Outline each Plasmodium falciparum-infected red blood cell.
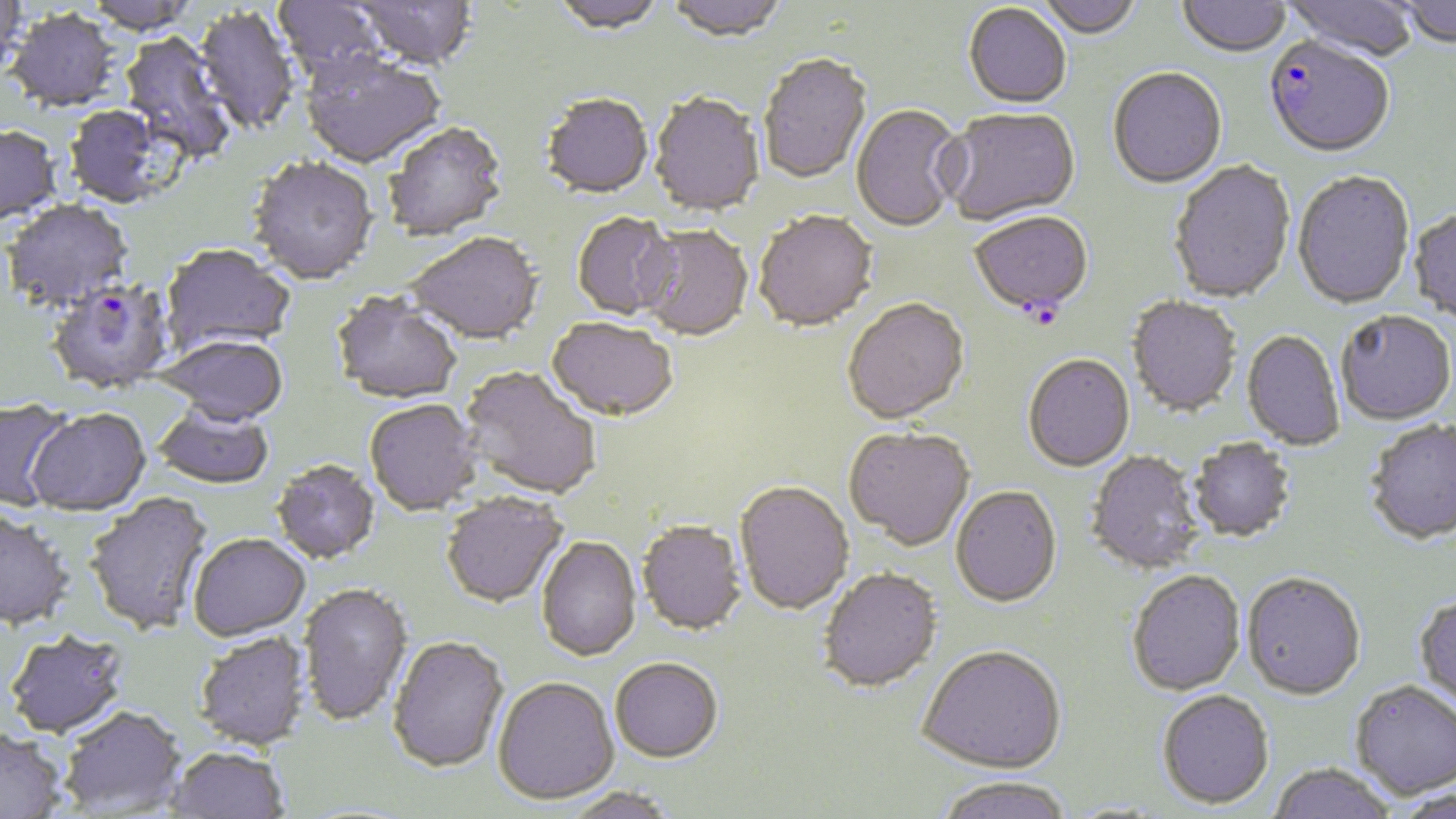
Approximate bounding boxes as [x1, y1, x2, y2] in pixels.
Plasmodium falciparum-infected red blood cells: [1263, 38, 1394, 161], [969, 214, 1094, 319], [47, 282, 176, 398].

slide_level_diagnosis: Plasmodium falciparum
image_size: 1456×819 pixels
magnification: 1000x
modality: optical microscopy
field_of_view: single
uninfected_red_blood_cell_locations: 'approximate bounding boxes as [x1, y1, x2, y2] in pixels: [271, 0, 387, 88], [351, 0, 479, 73], [550, 0, 667, 38], [665, 0, 791, 44], [1032, 0, 1145, 41], [1177, 0, 1291, 60], [1283, 0, 1419, 63], [1394, 0, 1456, 50], [0, 1, 28, 82], [963, 5, 1072, 111], [193, 7, 299, 138], [6, 11, 122, 115], [116, 33, 236, 164], [300, 54, 446, 171], [757, 56, 873, 186], [1107, 70, 1227, 191], [649, 94, 765, 219], [541, 96, 653, 201], [851, 105, 964, 234], [63, 106, 180, 210], [940, 109, 1081, 228], [385, 124, 508, 243], [0, 126, 63, 230], [247, 158, 379, 287], [1169, 162, 1296, 305], [1292, 172, 1415, 311], [3, 201, 134, 313], [1408, 208, 1456, 325], [754, 212, 878, 334], [572, 214, 679, 321], [638, 226, 753, 343], [408, 234, 543, 347], [160, 245, 295, 354], [330, 293, 463, 407], [1126, 297, 1241, 418], [843, 300, 970, 427], [1336, 313, 1456, 427], [547, 320, 678, 423], [1241, 331, 1345, 452], [157, 337, 288, 429], [1023, 355, 1135, 474], [459, 368, 601, 501], [0, 400, 75, 513], [365, 401, 483, 518], [153, 405, 274, 491], [26, 410, 151, 519], [1365, 421, 1456, 546], [843, 429, 974, 553], [1188, 439, 1297, 544], [1086, 452, 1206, 576], [271, 461, 380, 566], [734, 483, 854, 617], [951, 488, 1061, 610], [83, 492, 216, 638], [441, 493, 569, 610], [0, 510, 74, 633], [636, 522, 747, 637], [188, 536, 311, 644], [536, 538, 642, 663], [818, 569, 943, 696], [1127, 571, 1246, 697], [1242, 575, 1366, 702], [298, 584, 413, 728], [1413, 595, 1456, 713], [4, 632, 131, 741], [193, 633, 310, 752], [387, 637, 510, 775], [917, 648, 1067, 777], [610, 660, 722, 765], [493, 679, 619, 807], [1349, 682, 1456, 801], [1157, 692, 1275, 811], [57, 708, 188, 817], [0, 730, 67, 819], [164, 747, 289, 819], [1268, 764, 1396, 819], [934, 778, 1074, 819], [561, 789, 679, 819], [1388, 789, 1456, 818]'
preparation: thin blood film
stain: May-Grünwald-Giemsa